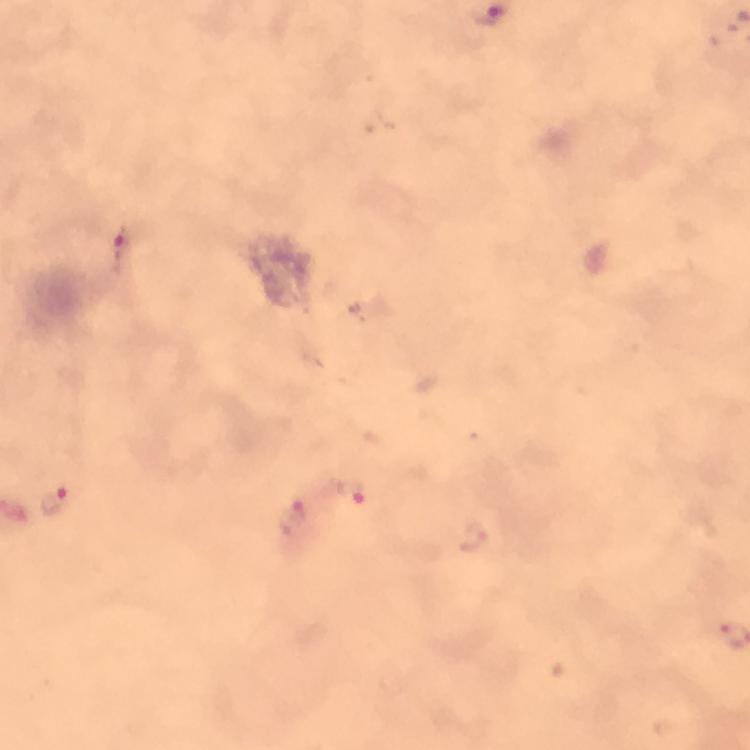
{
  "preparation": "thick smear",
  "magnification": "100x",
  "stain": "Giemsa",
  "image_size": "750×750 pixels",
  "capture": "smartphone camera through the microscope",
  "cropped_from": "one field of view",
  "immersion_oil": "used",
  "context": "from a malaria diagnostic workup",
  "malaria_parasite_locations": "approximate object centers, in pixels from the top-left corner: (x=121, y=254), (x=350, y=491), (x=54, y=501), (x=293, y=518), (x=474, y=534)"
}